Locate every leukocyte (white blood cell).
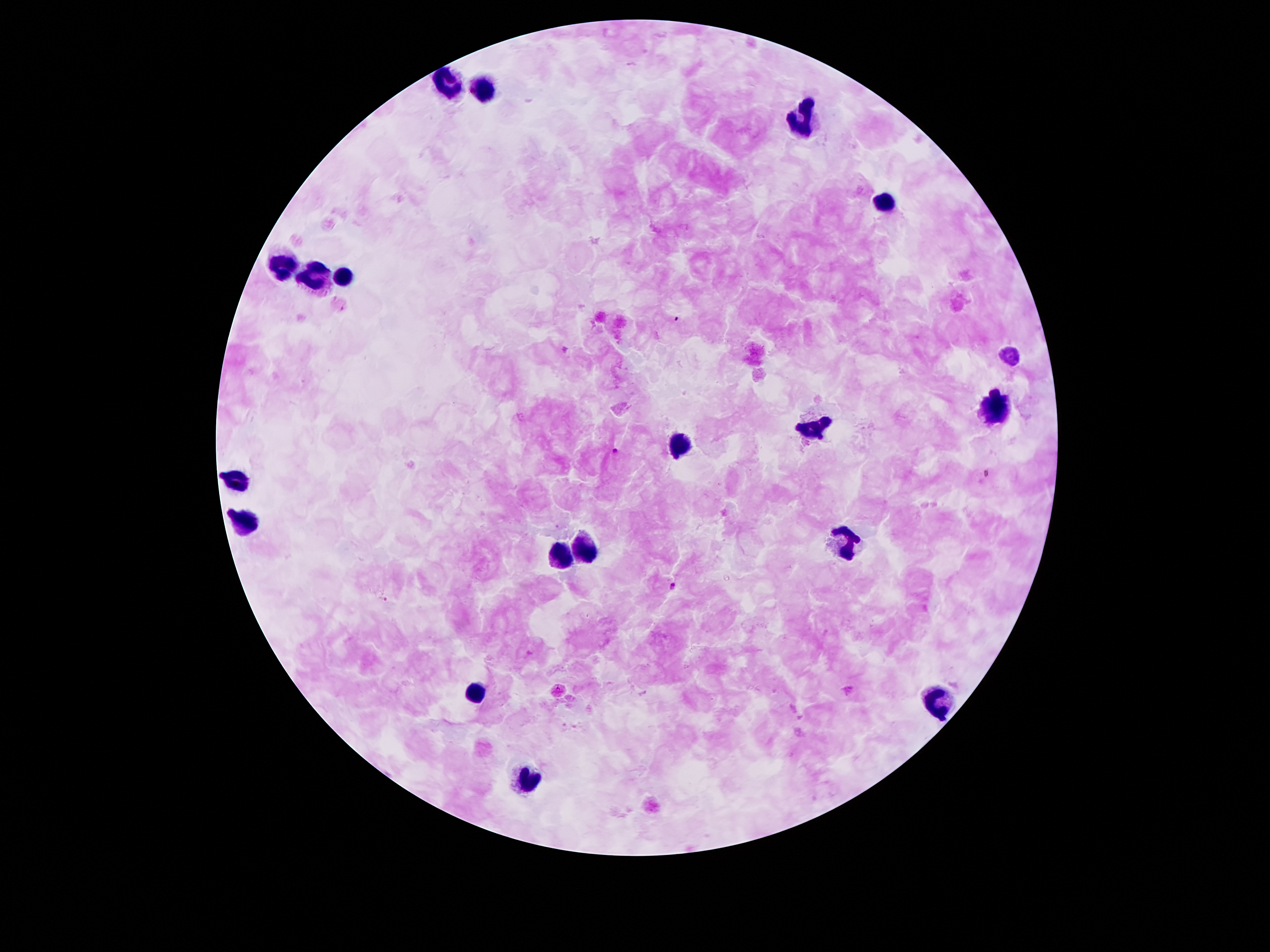

Approximate object centers, in pixels from the top-left corner.
Leukocytes: (x=445, y=85), (x=483, y=89), (x=805, y=125), (x=884, y=204), (x=285, y=264), (x=347, y=277), (x=320, y=280), (x=998, y=405), (x=813, y=426), (x=681, y=443), (x=239, y=481), (x=244, y=521), (x=841, y=547), (x=580, y=548), (x=559, y=558), (x=475, y=695), (x=936, y=700), (x=523, y=781).

Malaria parasite locations: (x=675, y=319), (x=614, y=452), (x=673, y=586), (x=386, y=600). 100x magnification. One field from this slide. Photographed through the microscope eyepiece with a smartphone camera. Thick blood smear. Patient malaria status: infected with Plasmodium falciparum. Giemsa-stained preparation. Image is 1270×952 pixels.